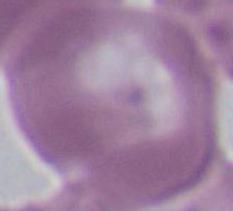

Summary:
  - Identification: red blood cell
  - Modality: photomicrograph
  - Magnification: 1000x